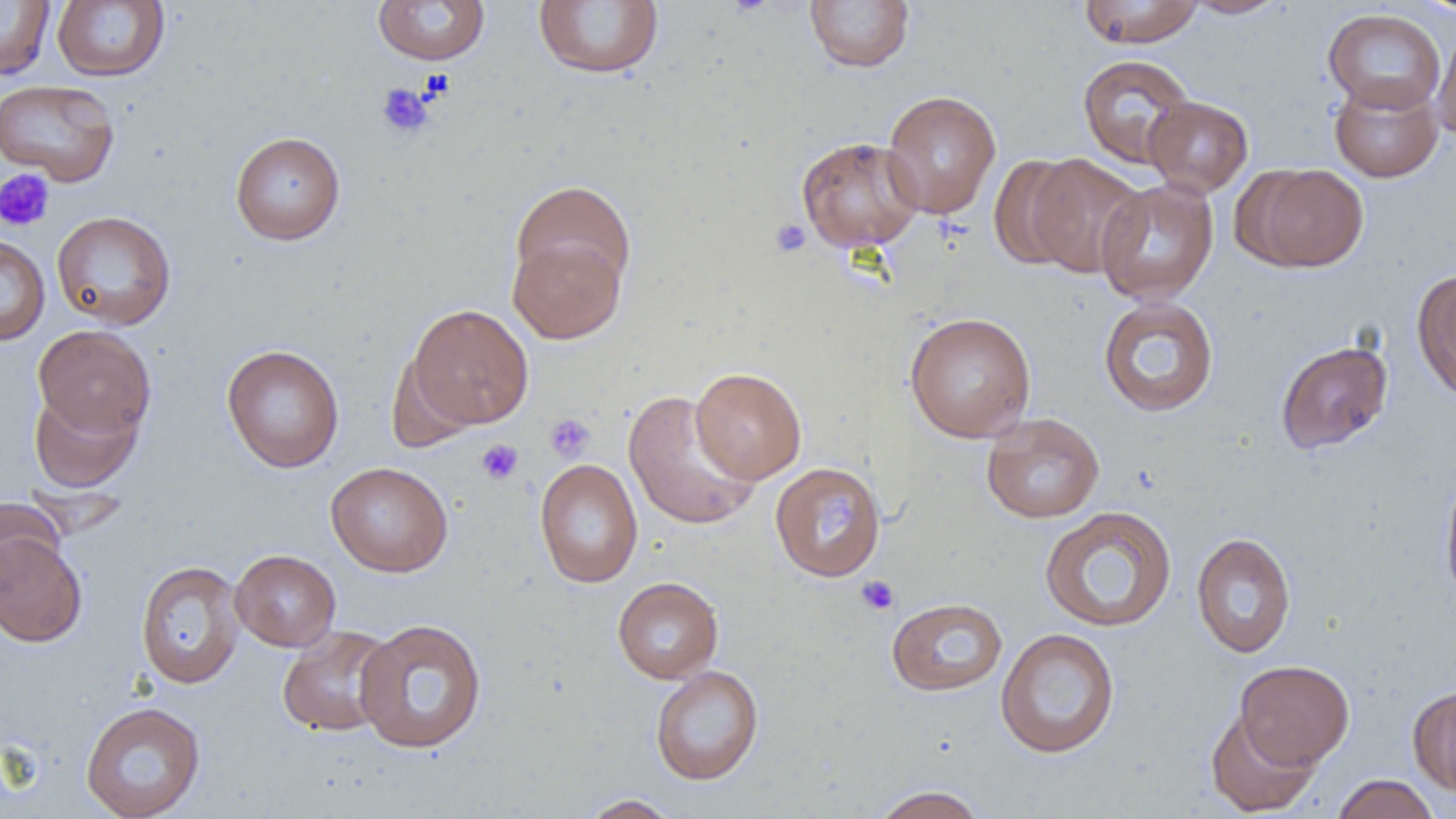 Approximate bounding boxes as (x1, y1, x2, y2) in pixels. Uninfected red blood cell locations: (0, 0, 55, 81), (372, 0, 491, 66), (532, 0, 665, 79), (805, 0, 915, 73), (1077, 0, 1206, 48), (1183, 0, 1290, 18), (1412, 0, 1456, 18), (51, 1, 170, 82), (1323, 8, 1446, 113), (1432, 25, 1456, 143), (1077, 54, 1197, 169), (1329, 75, 1444, 183), (0, 79, 120, 186), (881, 90, 1001, 219), (1144, 95, 1253, 197), (230, 131, 346, 245), (795, 135, 924, 253), (1024, 153, 1147, 278), (988, 154, 1090, 273), (1243, 163, 1369, 272), (510, 179, 636, 299), (1095, 179, 1218, 305), (51, 210, 177, 330), (508, 233, 627, 345), (0, 234, 50, 346), (1412, 267, 1456, 404), (1098, 295, 1219, 417), (406, 304, 534, 430), (904, 311, 1036, 443), (33, 324, 156, 439), (1275, 340, 1393, 455), (221, 344, 344, 473), (386, 351, 481, 451), (691, 367, 807, 484), (28, 388, 143, 493), (623, 390, 762, 531), (981, 412, 1104, 524), (534, 458, 643, 588), (326, 461, 453, 577), (769, 462, 885, 582), (1439, 469, 1456, 606), (0, 499, 64, 597), (1040, 506, 1177, 632), (0, 529, 88, 647), (1191, 531, 1296, 658), (230, 549, 341, 652), (135, 559, 246, 689), (612, 577, 723, 684), (886, 597, 1008, 696), (353, 618, 488, 754), (277, 625, 398, 737), (995, 628, 1121, 759), (1235, 659, 1354, 769), (650, 665, 764, 785), (1407, 685, 1456, 796), (80, 701, 206, 819), (1204, 707, 1321, 817), (1329, 774, 1441, 819), (871, 784, 988, 819), (577, 794, 682, 818). Platelet locations: (376, 82, 434, 138), (0, 168, 55, 232), (768, 217, 812, 259), (545, 413, 595, 462), (476, 440, 524, 485), (855, 575, 899, 616). Slide-level diagnosis: negative for blood parasites. Thin blood film. Image is 1456×819 pixels. 1000x magnification. Optical microscopy. Single field of view.